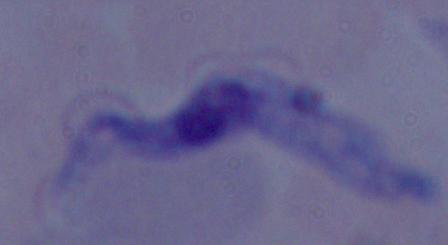
Summary:
  - Identification: trypanosome
  - Magnification: 1000x
  - Modality: micrograph